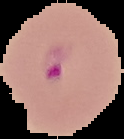 From a thin blood film. Image is 124×139 pixels. The area outside the segmented cell region is set to black. Result: Plasmodium parasites detected.